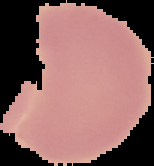 From a thin blood smear. Malaria status: uninfected. The area outside the segmented cell region is set to black. Image is 154×166 pixels.